Outline each Plasmodium malariae-infected red blood cell.
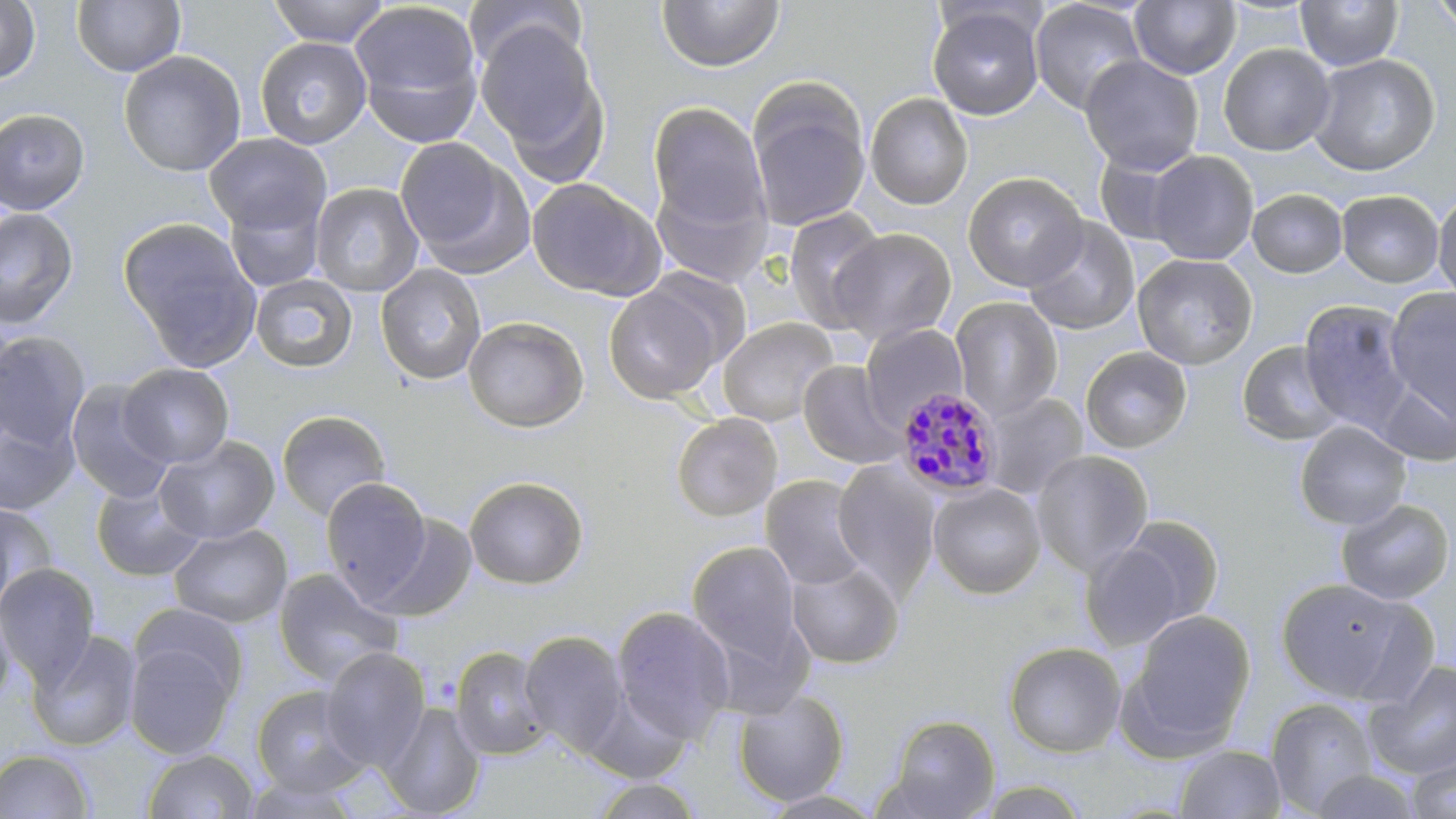
Approximate bounding boxes as (x1, y1, x2, y2) in pixels.
Plasmodium malariae-infected red blood cells: (895, 387, 1003, 498).

Summary:
  - Uninfected red blood cell locations: (0, 0, 40, 83), (72, 0, 186, 77), (269, 0, 390, 47), (655, 0, 784, 72), (1029, 0, 1148, 115), (1429, 0, 1456, 36), (348, 1, 484, 141), (1130, 1, 1241, 79), (1295, 1, 1403, 71), (927, 5, 1044, 120), (475, 18, 609, 177), (255, 37, 372, 149), (1218, 43, 1335, 156), (118, 50, 246, 177), (1308, 54, 1440, 176), (1079, 55, 1204, 175), (746, 82, 871, 232), (865, 93, 973, 210), (647, 101, 771, 238), (0, 108, 90, 215), (204, 132, 331, 236), (394, 136, 527, 271), (1146, 150, 1259, 265), (963, 171, 1089, 293), (527, 177, 664, 300), (309, 183, 424, 297), (1248, 188, 1348, 277), (1336, 189, 1445, 287), (1432, 189, 1456, 306), (224, 194, 326, 294), (0, 207, 78, 330), (782, 208, 888, 331), (1022, 217, 1140, 335), (119, 219, 258, 367), (828, 228, 957, 345), (1133, 254, 1257, 369), (375, 262, 487, 385), (250, 274, 358, 373), (604, 282, 726, 404), (1385, 288, 1456, 422), (950, 297, 1062, 419), (1298, 299, 1415, 435), (463, 316, 589, 432), (716, 316, 839, 426), (859, 323, 968, 429), (0, 331, 91, 450), (1236, 341, 1346, 447), (1080, 346, 1193, 453), (798, 360, 907, 469), (117, 363, 234, 469), (1376, 374, 1456, 467), (65, 379, 173, 504), (980, 391, 1089, 499), (0, 409, 79, 516), (276, 409, 391, 521), (671, 413, 783, 522), (1294, 420, 1412, 530), (155, 436, 279, 544), (1031, 449, 1154, 577), (832, 459, 940, 596), (463, 475, 589, 590), (760, 475, 871, 591), (320, 478, 432, 602), (91, 479, 205, 582), (928, 482, 1046, 600), (1335, 498, 1455, 604), (0, 500, 57, 610), (367, 513, 478, 622), (1110, 515, 1225, 632), (168, 523, 293, 628), (1079, 536, 1196, 650), (686, 540, 805, 673), (785, 558, 904, 669), (0, 563, 100, 685), (272, 567, 403, 687), (1275, 578, 1416, 703), (610, 605, 735, 746), (0, 606, 15, 709), (1122, 608, 1256, 754), (123, 624, 242, 760), (26, 629, 141, 751), (518, 630, 632, 758), (1003, 641, 1126, 758), (451, 645, 553, 760), (320, 647, 432, 771), (1364, 659, 1456, 781), (250, 684, 372, 797), (732, 688, 850, 806), (1265, 697, 1380, 816), (380, 702, 486, 818), (883, 714, 1001, 818), (1174, 744, 1286, 818), (0, 749, 94, 818), (143, 749, 258, 818), (1404, 751, 1456, 819), (1306, 769, 1425, 818), (240, 775, 364, 818), (589, 777, 705, 818), (969, 781, 1093, 819), (756, 790, 889, 818)
  - Slide-level diagnosis: Plasmodium malariae
  - Magnification: 1000x
  - Stain: May-Grünwald-Giemsa
  - Image size: 1456×819 pixels
  - Modality: light microscopy
  - Field of view: one of a larger specimen
  - Preparation: thin blood smear